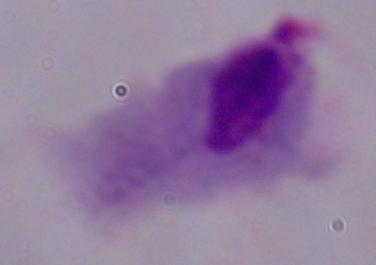
1000x magnification. A trichomonad is shown. Photomicrograph.